Evaluate for Plasmodium parasites.
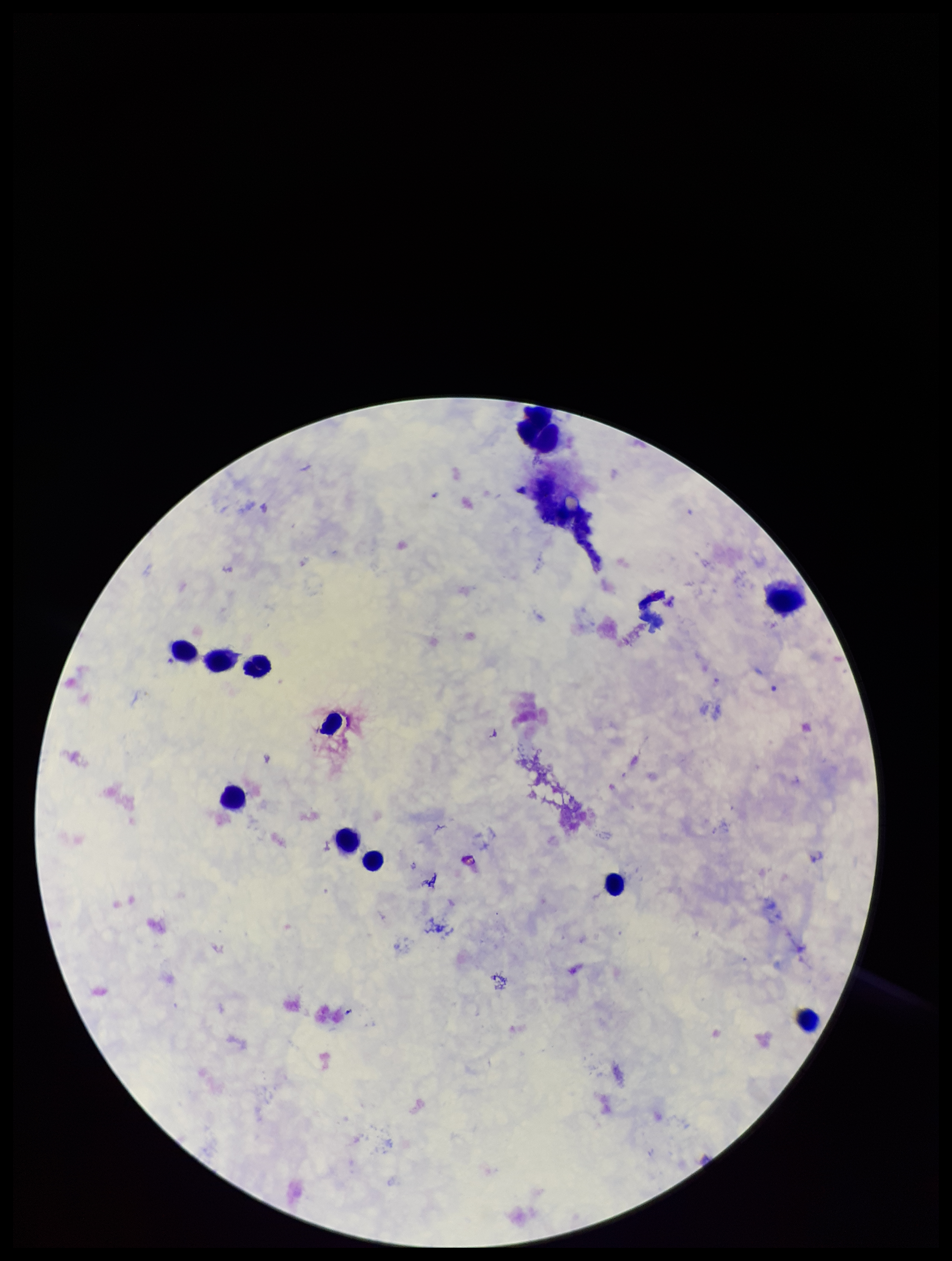
None seen.

Stained with Giemsa. Leukocyte count: 11. One field from this slide. Species reported for this patient: Plasmodium falciparum. Preparation: thick smear. Smartphone photograph taken through the eyepiece of a microscope. Patient malaria status: infected. Image is 952×1261 pixels. Parasite count: 0.